Point out each Plasmodium parasite.
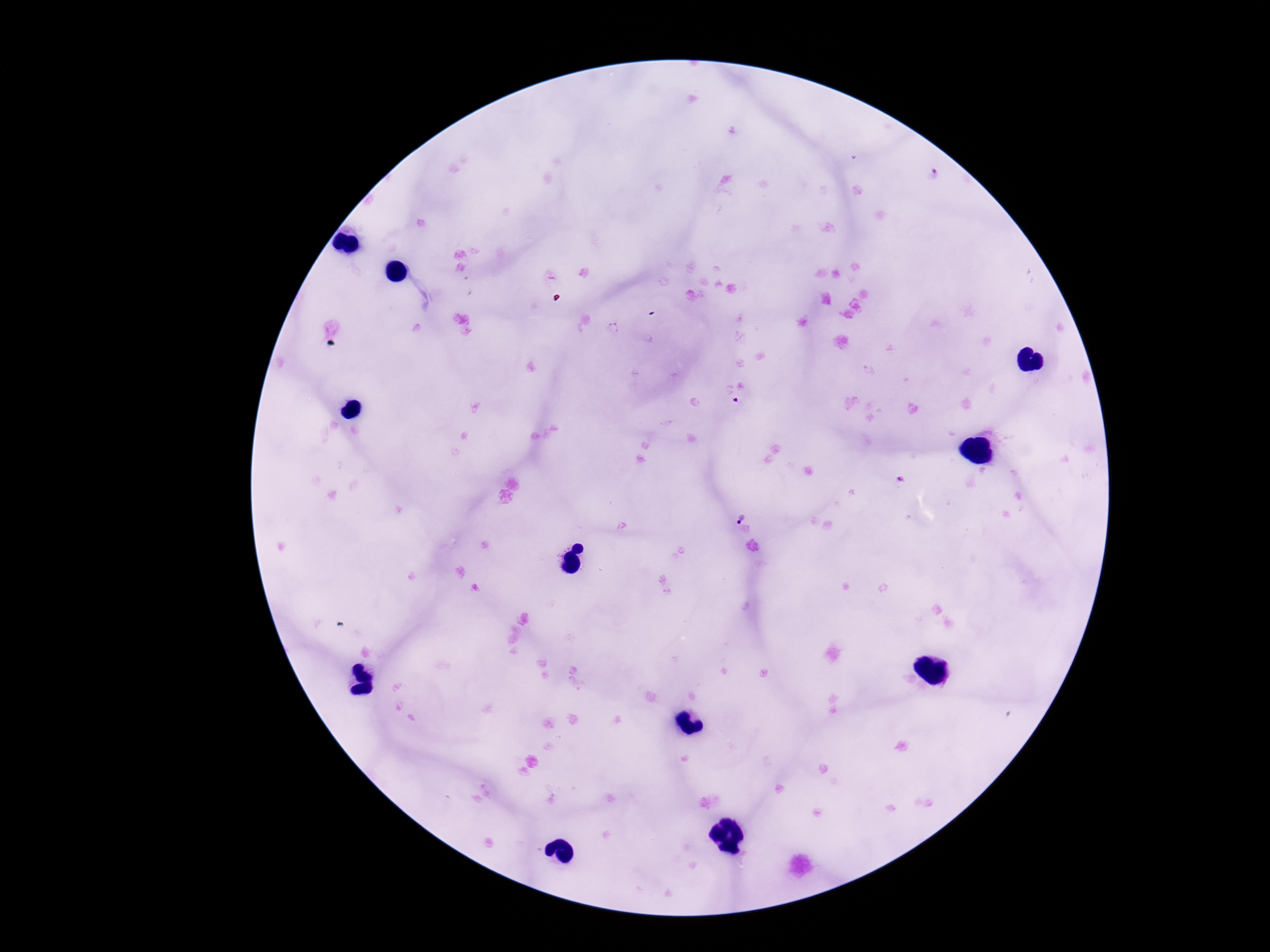

Approximate centers as [x, y] in pixels.
Plasmodium parasites: [932, 174], [737, 401], [745, 509].

magnification = 100x
preparation = thick blood smear
patient malaria status = positive
capture = smartphone camera through the microscope eyepiece
image size = 1270×952 pixels
field of view = one from this slide
stain = Giemsa